Assess this cell for malaria.
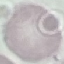
It is uninfected.

Acquired by smartphone through the microscope eyepiece. Thin blood smear. Giemsa-stained preparation. Automatically extracted cell patch, resized to 64 × 64 pixels.